Describe the morphology of the erythrocytes.
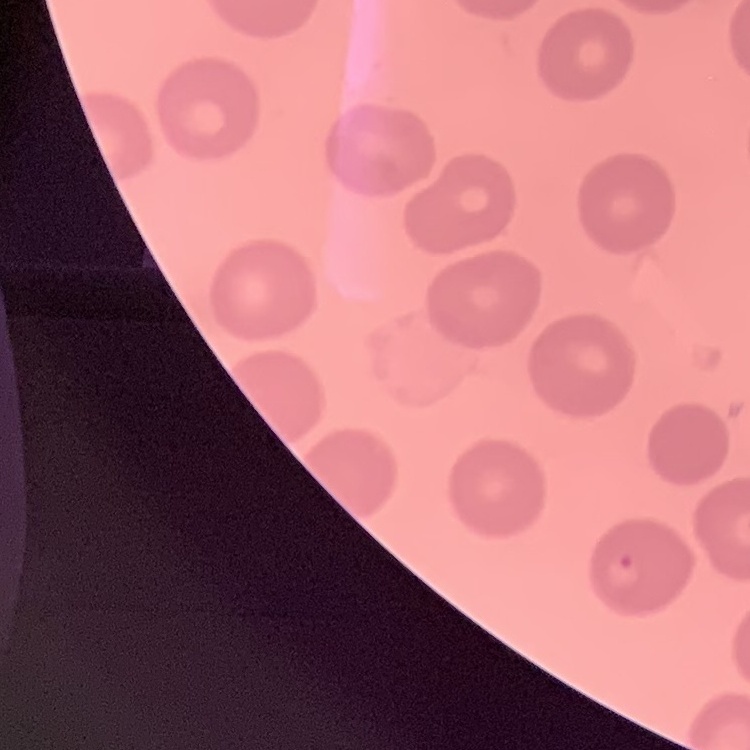
No rouleaux formation.

Thin peripheral smear. Stained with either Field's or Giemsa. One tile cut from a larger photomicrograph.